Classify this cell by malaria status.
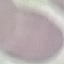

It is uninfected.

Summary:
  - Capture: smartphone through the microscope eyepiece
  - Image type: cell patch, automatically extracted from a larger field of view and resized to 64 × 64 pixels
  - Preparation: thin smear
  - Stain: Giemsa